Describe the morphology of the red blood cells.
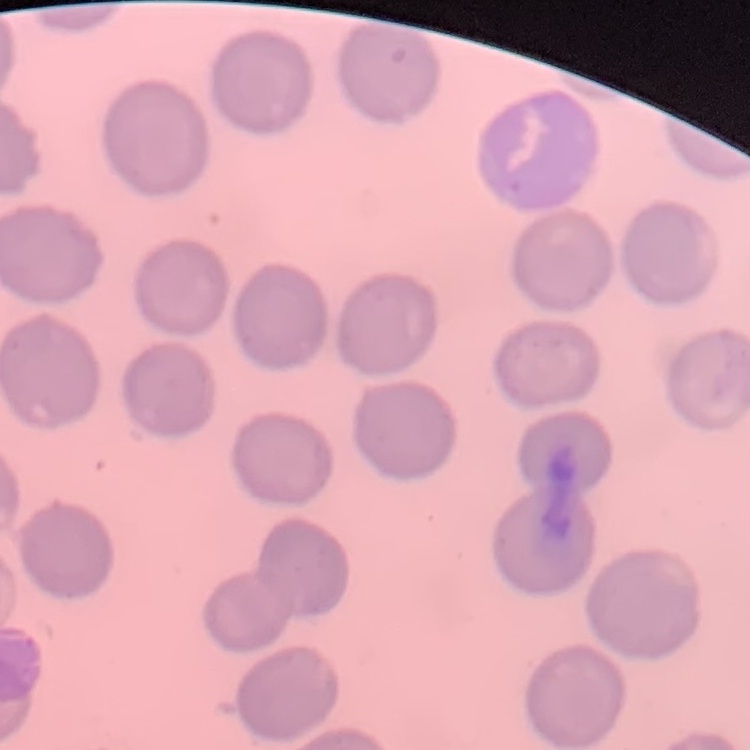
They show no rouleaux formation.

Summary:
  - Preparation: thin blood film
  - Stain: Field's or Giemsa
  - Image type: square crop of a larger photomicrograph